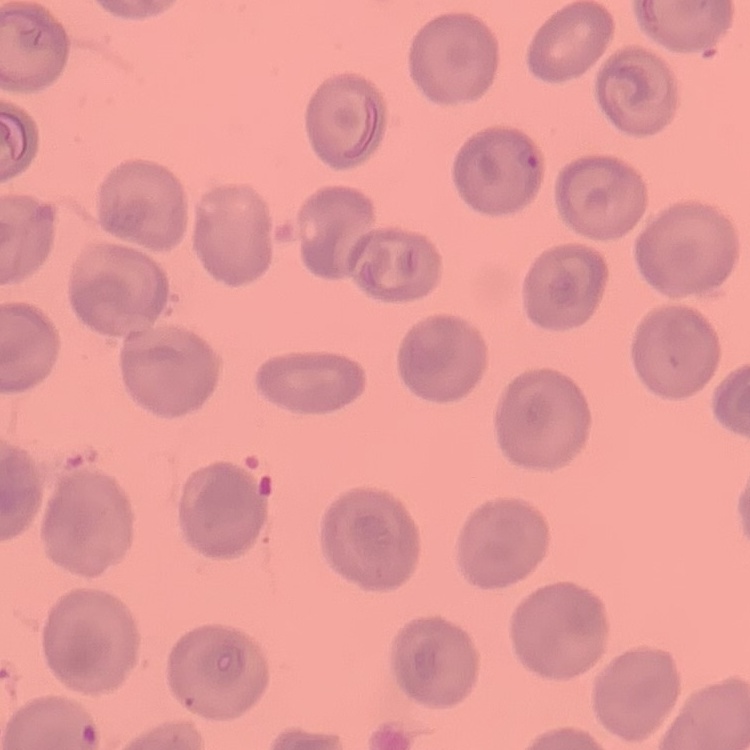

Summary:
  - Red blood cell morphology: no rouleaux formation
  - Preparation: thin blood smear
  - Stain: Field's or Giemsa
  - Image type: square crop of a larger photomicrograph